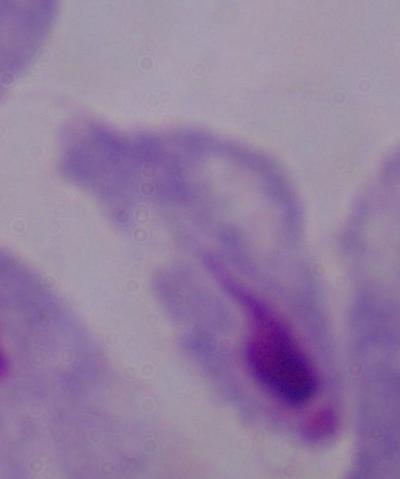
Summary:
  - Identification: trichomonad
  - Modality: micrograph
  - Magnification: 1000x